State the blood parasite species.
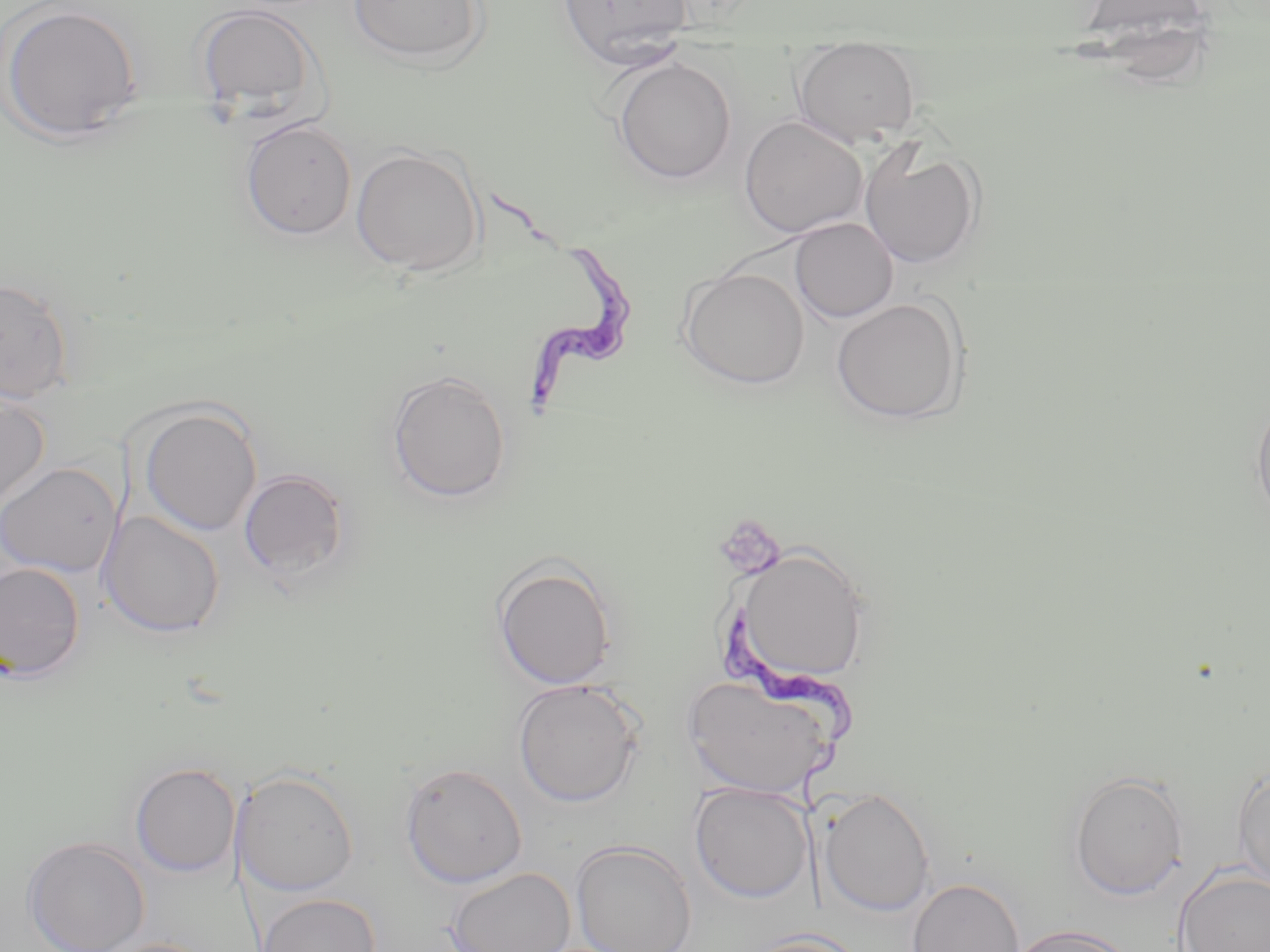

Trypanosoma brucei.

{
  "magnification": "1000x",
  "trypanosoma_brucei_locations": "approximate bounding boxes as (x1, y1, x2, y2) in pixels: (489, 192, 638, 433), (713, 608, 858, 817)",
  "preparation": "thin blood film",
  "uninfected_red_blood_cell_locations": "approximate bounding boxes as (x1, y1, x2, y2) in pixels: (346, 0, 490, 69), (1, 1, 147, 145), (556, 1, 694, 68), (193, 3, 326, 121), (792, 44, 922, 147), (612, 57, 737, 184), (738, 116, 869, 239), (239, 118, 358, 240), (859, 143, 984, 270), (351, 146, 485, 276), (790, 217, 898, 323), (677, 267, 810, 390), (0, 276, 74, 405), (830, 297, 967, 425), (387, 370, 512, 503), (0, 387, 50, 511), (1250, 395, 1270, 524), (137, 403, 262, 536), (0, 462, 121, 578), (238, 468, 351, 582), (99, 511, 226, 638), (728, 545, 873, 689), (492, 557, 617, 690), (0, 561, 86, 682), (682, 671, 840, 799), (512, 679, 644, 806), (129, 761, 241, 877), (399, 762, 528, 888), (1232, 762, 1270, 894), (232, 769, 360, 896), (1068, 770, 1189, 901), (690, 782, 813, 903), (818, 787, 935, 916), (23, 836, 150, 952), (570, 840, 697, 952), (1174, 865, 1270, 952), (444, 867, 576, 952), (906, 877, 1026, 952), (256, 892, 381, 952), (1007, 923, 1137, 952), (739, 930, 870, 952), (99, 938, 218, 952)",
  "stain": "May-Grünwald-Giemsa",
  "image_size": "1270×952 pixels",
  "modality": "light microscopy",
  "field_of_view": "one of a larger specimen"
}